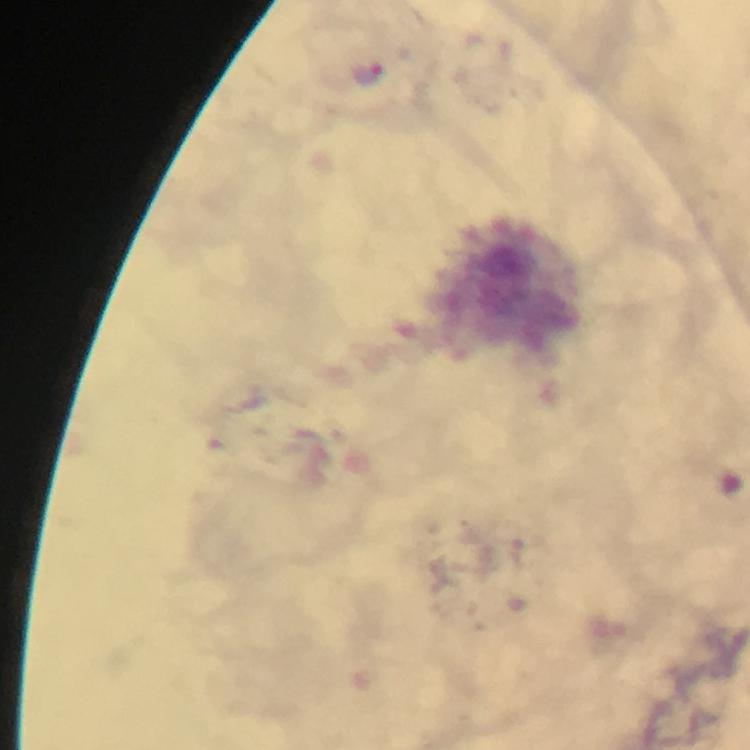
Approximate centers as [x, y] in pixels.
Summary:
  - Malaria parasite locations: [369, 73]
  - Preparation: thick smear
  - Context: from a diagnostic examination for malaria
  - Stain: Giemsa
  - Immersion oil: applied
  - Cropped from: one field of view
  - Magnification: 100x
  - Image size: 750×750 pixels
  - Capture: smartphone mounted on the microscope